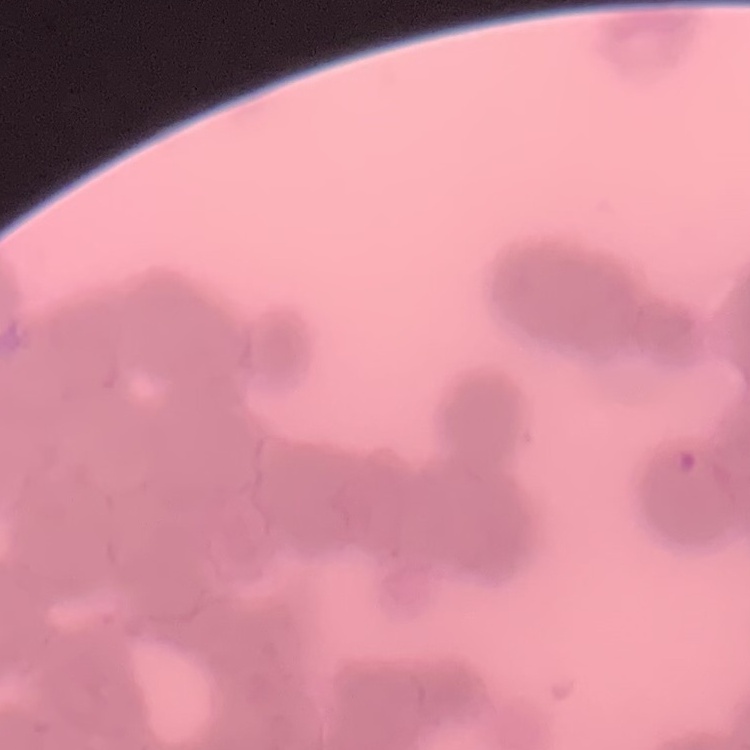

The red blood cells show rouleaux formation. Field's or Giemsa stain. Square crop of a larger photomicrograph. Thin peripheral smear.